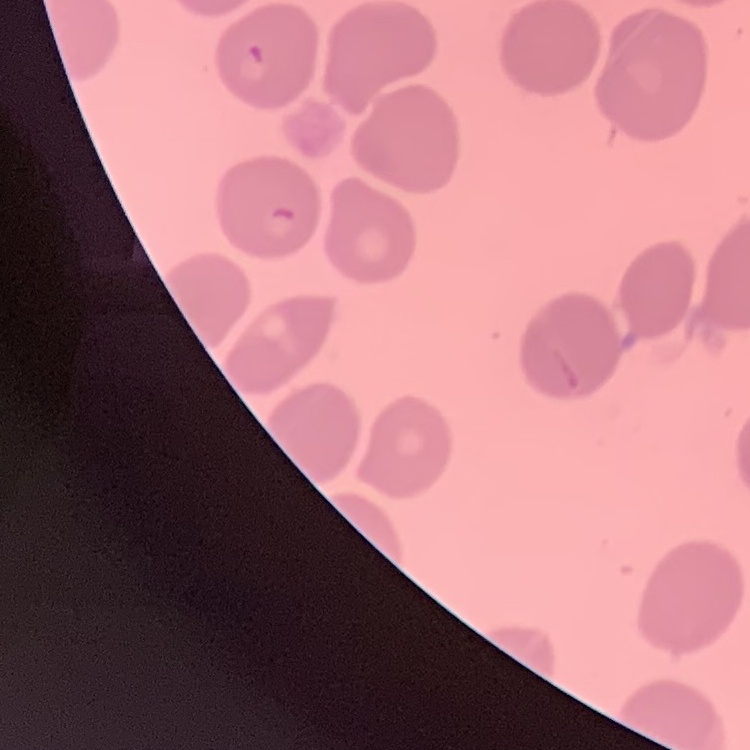

The red blood cells show no rouleaux formation. Square crop of a larger photomicrograph. Thin blood film. Stained with either Field's or Giemsa.